Classify this cell by malaria status.
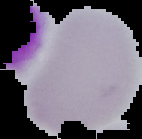
It is uninfected.

From a thin blood smear. Image is 142×139 pixels. The area outside the segmented cell region is set to black.